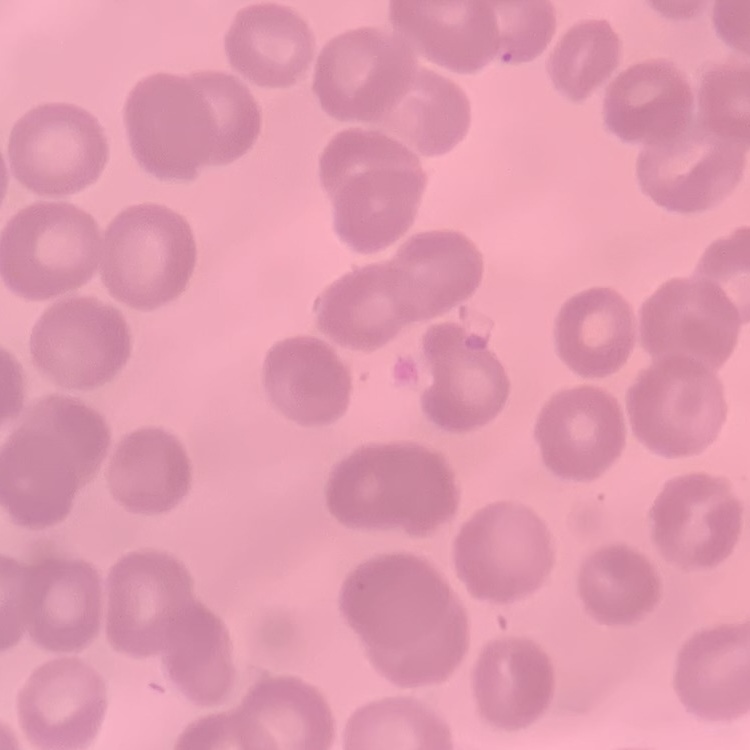
The red blood cells show no rouleaux formation. One tile cut from a larger photomicrograph. Field's or Giemsa stain. Thin blood film.